Locate and identify every blood parasite.
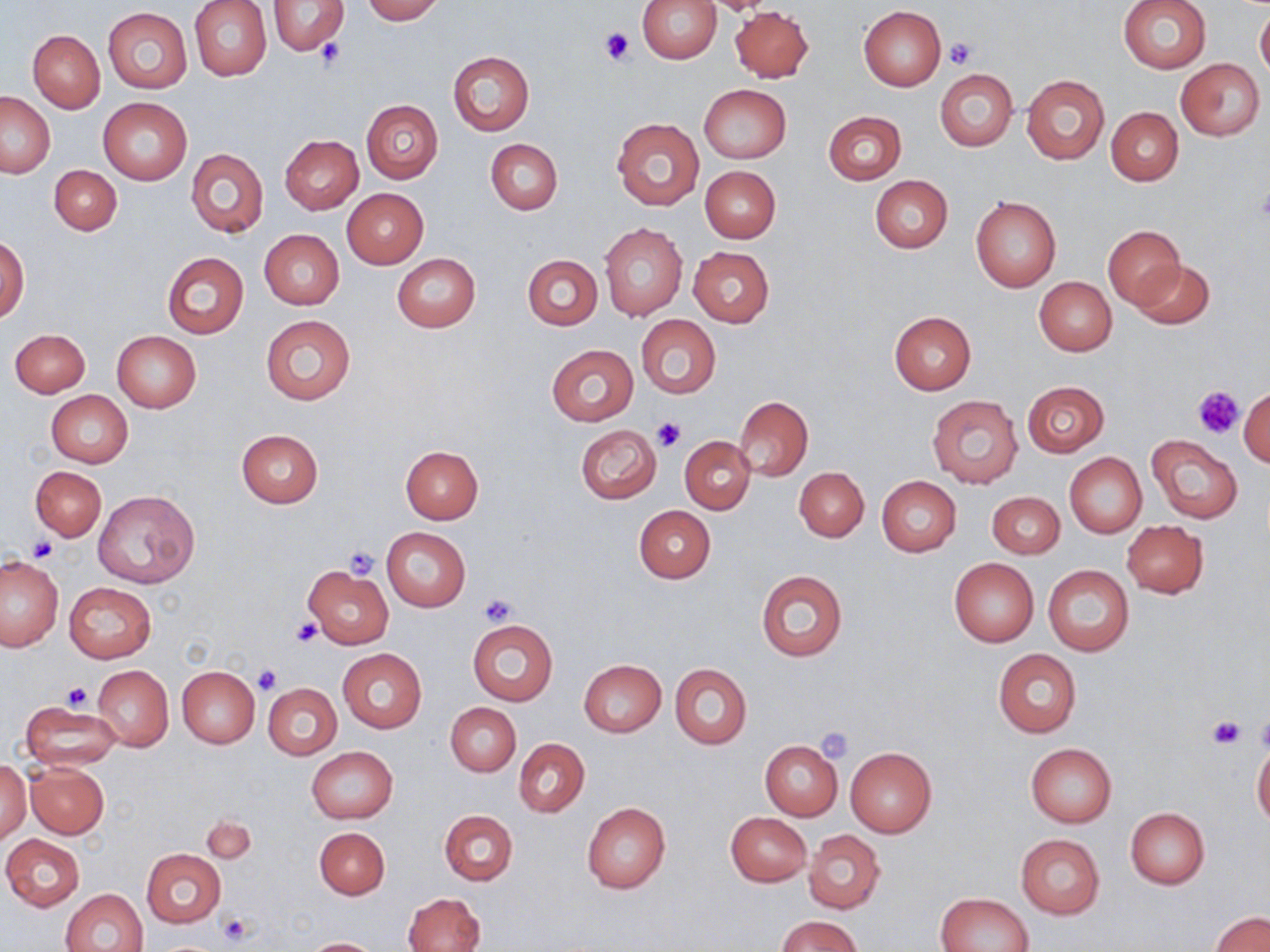
No blood parasites observed.

Summary:
  - Coordinate format: approximate bounding boxes as (x1,y1)-(x2,y2) corner pairs in pixels
  - Platelet locations: (600,27)-(634,64), (316,39)-(345,68), (946,39)-(977,67), (1194,385)-(1242,437), (652,418)-(686,454), (28,539)-(57,563), (343,546)-(380,578), (478,593)-(517,626), (292,616)-(320,646), (252,664)-(280,694), (61,680)-(93,710), (1256,713)-(1270,752), (1208,715)-(1244,751), (815,728)-(854,764), (218,913)-(252,945)
  - Uninfected red blood cell locations: (190,0)-(272,81), (362,0)-(443,23), (638,0)-(721,63), (703,0)-(778,17), (1118,0)-(1211,73), (267,1)-(348,55), (858,5)-(946,90), (731,6)-(814,82), (103,8)-(192,94), (1255,9)-(1270,80), (29,30)-(105,112), (448,51)-(535,135), (1176,58)-(1266,141), (935,68)-(1017,151), (1021,74)-(1109,165), (698,84)-(790,163), (0,90)-(55,178), (99,98)-(192,184), (362,100)-(443,183), (1107,107)-(1184,185), (823,110)-(905,185), (612,116)-(704,211), (280,135)-(363,214), (486,138)-(563,215), (187,148)-(268,237), (49,164)-(121,236), (700,166)-(781,243), (869,175)-(953,254), (342,188)-(428,269), (971,196)-(1061,292), (599,224)-(687,321), (1103,226)-(1184,305), (259,229)-(345,310), (1,233)-(29,322), (687,246)-(774,326), (161,252)-(249,340), (392,253)-(481,332), (523,254)-(602,329), (1130,258)-(1215,329), (1034,276)-(1116,355), (889,311)-(976,394), (260,314)-(355,406), (636,314)-(720,399), (10,328)-(90,397), (111,331)-(201,413), (546,345)-(638,424), (1022,380)-(1109,456), (1239,384)-(1270,467), (42,390)-(120,541), (46,390)-(133,467), (928,395)-(1023,488), (734,396)-(812,480), (574,425)-(662,505), (236,428)-(324,507), (1146,435)-(1243,523), (680,436)-(756,513), (400,446)-(484,524), (1065,453)-(1145,537), (31,467)-(105,541), (794,467)-(868,541), (876,476)-(961,557), (93,489)-(200,589), (987,491)-(1064,559), (634,505)-(715,583), (1120,520)-(1207,598), (382,528)-(470,611), (0,556)-(64,653), (949,557)-(1039,647), (1042,563)-(1134,656), (304,564)-(392,648), (756,570)-(847,661), (64,582)-(156,663), (467,619)-(558,705), (338,648)-(427,734), (993,648)-(1081,738), (579,659)-(666,736), (669,663)-(751,750), (93,665)-(173,751), (178,666)-(259,747), (264,683)-(341,760), (19,701)-(121,771), (446,703)-(520,776), (513,738)-(590,818), (759,739)-(843,821), (1025,742)-(1117,827), (1252,743)-(1270,827), (306,746)-(398,823), (845,747)-(937,836), (1,757)-(31,844), (25,762)-(108,838), (581,802)-(671,894), (1124,807)-(1210,889), (440,810)-(518,886), (725,811)-(811,887), (201,816)-(255,862), (314,826)-(389,899), (804,830)-(885,914), (2,834)-(85,912), (1016,834)-(1105,918), (141,849)-(226,927), (61,889)-(148,952), (402,891)-(485,952), (936,892)-(1033,952), (1209,911)-(1270,952), (778,916)-(864,952), (303,937)-(384,952)
  - Slide-level diagnosis: negative for blood parasites
  - Modality: optical microscopy
  - Image size: 1270×952 pixels
  - Field of view: single
  - Stain: May-Grünwald-Giemsa
  - Magnification: 1000x
  - Preparation: thin blood film